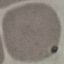
Summary:
  - Malaria status: uninfected
  - Preparation: thin blood film
  - Image type: cell patch, automatically extracted from a larger field of view and resized to 64 × 64 pixels
  - Capture: smartphone camera at the microscope eyepiece
  - Stain: Giemsa